Locate every Plasmodium parasite.
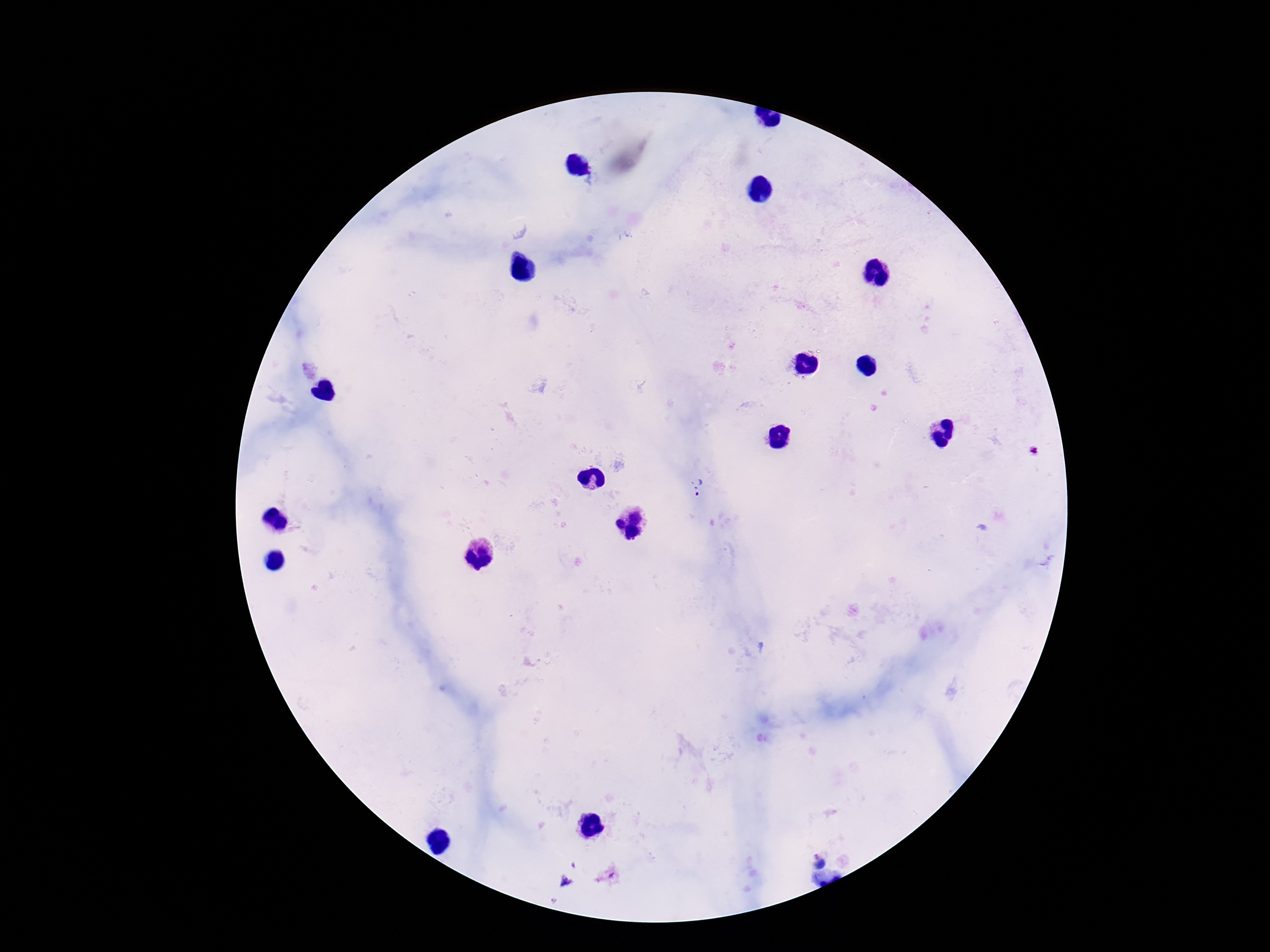

Approximate object centers, in pixels from the top-left corner.
Plasmodium parasites: (x=699, y=487), (x=818, y=859), (x=565, y=881).

Summary:
  - Field of view: single
  - Preparation: thick peripheral-blood smear
  - Magnification: 100x
  - Image size: 1270×952 pixels
  - Capture: smartphone camera through the microscope eyepiece
  - Stain: Giemsa
  - Patient malaria status: infected